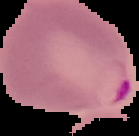
{
  "image_size": "139×136 pixels",
  "malaria_status": "parasitized",
  "preparation": "thin blood film",
  "image_type": "cell region segmented out of the field of view; surrounding area masked to black"
}